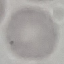
result = no malaria parasites detected
stain = Giemsa
capture = smartphone camera at the microscope eyepiece
preparation = thin blood smear
image type = cell patch, automatically extracted from a larger field of view and resized to 64 × 64 pixels